Give the position of every malaria parasite.
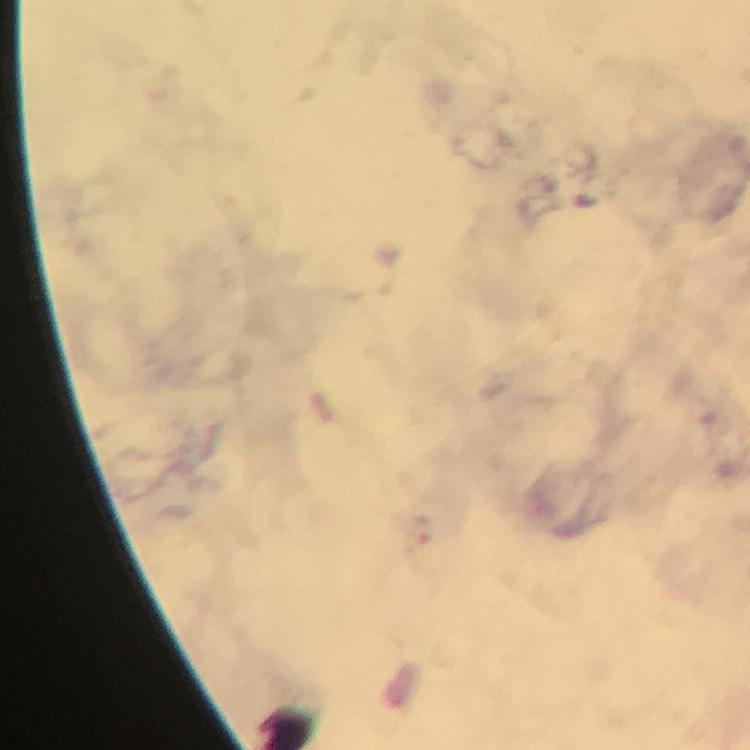
Approximate centers as (x, y) in pixels.
Malaria parasites: (420, 530).

Summary:
  - Capture: smartphone mounted on the microscope
  - Stain: Giemsa
  - Preparation: thick smear
  - Immersion oil: used
  - Cropped from: a single field of view
  - Context: from a malaria diagnostic workup
  - Magnification: 100x
  - Image size: 750×750 pixels